State which parasite is depicted.
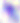
This is Toxoplasma gondii.

Photomicrograph. Captured at 400x magnification.